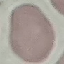

result: no malaria parasites seen
preparation: thin blood film
stain: Giemsa
image_type: automatically extracted cell patch, resized to 64 × 64 pixels
capture: smartphone through the microscope eyepiece